Assess this cell for malaria.
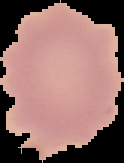
It is uninfected.

image type = cell region segmented out of the field of view; surrounding area masked to black
image size = 124×163 pixels
preparation = thin blood smear